Identify the parasite.
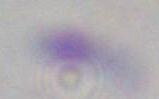

Toxoplasma gondii.

1000x magnification. Photomicrograph.